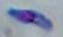

modality = photomicrograph
identification = Toxoplasma gondii
magnification = 1000x